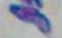
Summary:
  - Identification: Toxoplasma gondii
  - Modality: micrograph
  - Magnification: 1000x